Report the malaria status of this cell.
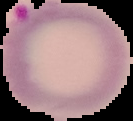

It is parasitized.

Summary:
  - Image size: 133×121 pixels
  - Image type: segmented cell region on a black background
  - Preparation: thin blood film